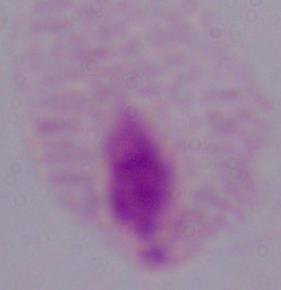 1000x magnification. Photomicrograph. A trichomonad is shown.